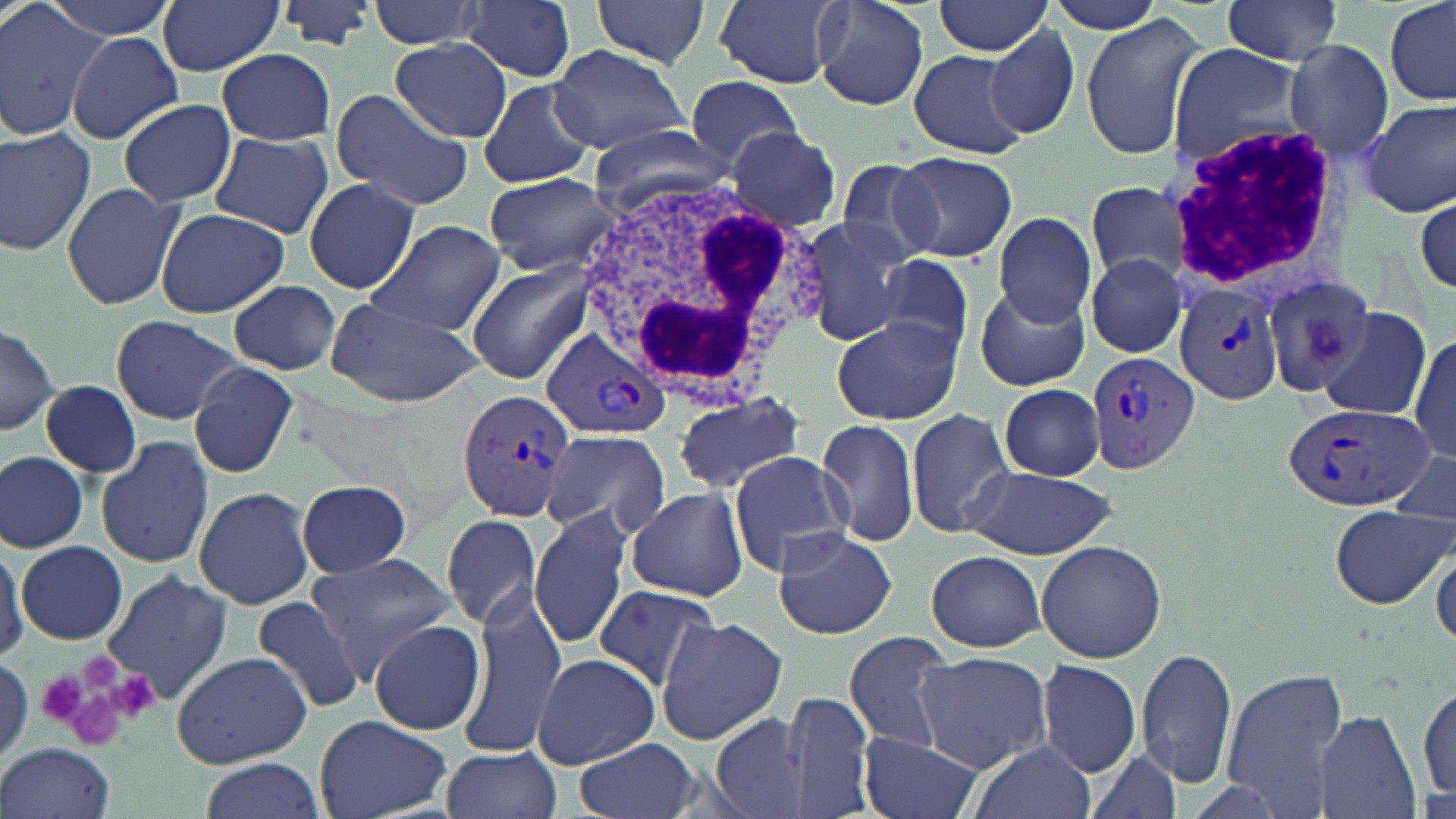

Approximate bounding boxes as (x1,y1)-(x2,y2) corner pairs in pixels. Platelet locations: (36,669)-(90,725), (110,669)-(159,720), (52,679)-(141,754). Uninfected red blood cell locations: (0,0)-(108,142), (46,0)-(179,40), (157,0)-(282,76), (275,0)-(379,52), (368,0)-(487,50), (462,0)-(578,82), (592,0)-(712,68), (714,0)-(845,88), (813,0)-(931,113), (1045,0)-(1168,35), (1220,0)-(1346,63), (1385,0)-(1455,105), (932,2)-(1053,58), (1080,13)-(1208,163), (986,25)-(1081,140), (67,31)-(186,145), (389,39)-(513,142), (1284,39)-(1391,159), (549,44)-(690,154), (1165,44)-(1309,174), (218,48)-(336,144), (907,49)-(1031,159), (684,77)-(808,168), (477,78)-(595,189), (329,90)-(473,211), (116,98)-(237,208), (1363,100)-(1455,218), (0,125)-(98,256), (587,125)-(730,208), (724,127)-(841,230), (210,133)-(335,238), (892,151)-(1017,262), (834,157)-(950,266), (485,171)-(619,275), (303,178)-(420,295), (1085,180)-(1196,288), (61,181)-(187,311), (1414,188)-(1456,300), (153,207)-(291,316), (993,214)-(1098,325), (798,218)-(911,347), (365,219)-(507,337), (874,253)-(976,358), (1084,254)-(1188,357), (465,260)-(596,385), (1264,271)-(1376,390), (228,279)-(342,375), (974,285)-(1090,390), (324,297)-(483,408), (1315,308)-(1428,416), (110,314)-(241,424), (832,316)-(961,426), (0,323)-(59,437), (1409,332)-(1456,465), (188,361)-(298,479), (42,380)-(141,477), (1000,384)-(1105,480), (671,392)-(806,495), (906,408)-(1015,539), (816,418)-(919,547), (540,428)-(670,539), (94,434)-(215,570), (726,450)-(852,577), (1386,450)-(1456,528), (0,452)-(87,553), (961,465)-(1115,557), (298,480)-(414,578), (194,484)-(316,609), (627,485)-(748,602), (1328,504)-(1451,608), (530,507)-(633,649), (442,513)-(543,630), (772,530)-(897,639), (0,536)-(27,665), (1035,540)-(1167,662), (18,541)-(130,645), (926,549)-(1046,653), (1431,549)-(1455,651), (306,552)-(455,677), (101,569)-(234,704), (591,584)-(724,694), (461,587)-(574,744), (251,595)-(368,715), (658,617)-(787,743), (369,619)-(486,735), (842,631)-(956,755), (1137,646)-(1238,787), (172,651)-(313,768), (913,652)-(1052,770), (531,653)-(660,768), (1038,658)-(1141,777), (1223,669)-(1348,808), (1416,682)-(1454,806), (780,688)-(876,819), (1314,710)-(1420,819), (711,713)-(807,819), (316,715)-(452,819), (857,730)-(984,819), (575,737)-(700,819), (966,741)-(1098,819), (1,742)-(117,819), (440,745)-(562,819), (1084,748)-(1183,819), (202,758)-(323,817). Plasmodium vivax-infected red blood cell locations: (1172,283)-(1283,406), (543,327)-(672,438), (1088,351)-(1200,471), (457,390)-(576,520), (1281,403)-(1432,512). White blood cell locations: (1168,125)-(1337,286), (569,170)-(807,396). Slide-level diagnosis: Plasmodium vivax. Optical microscopy. Captured at 1000x magnification. Image is 1456×819 pixels. One field of a larger specimen. Thin blood smear. May-Grünwald-Giemsa stain.